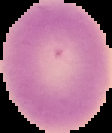

image type = cell region segmented out of the field of view; surrounding area masked to black
image size = 112×133 pixels
result = no malaria parasites detected
preparation = thin blood film